Identify the parasite.
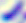

Toxoplasma gondii.

Summary:
  - Magnification: 400x
  - Modality: photomicrograph